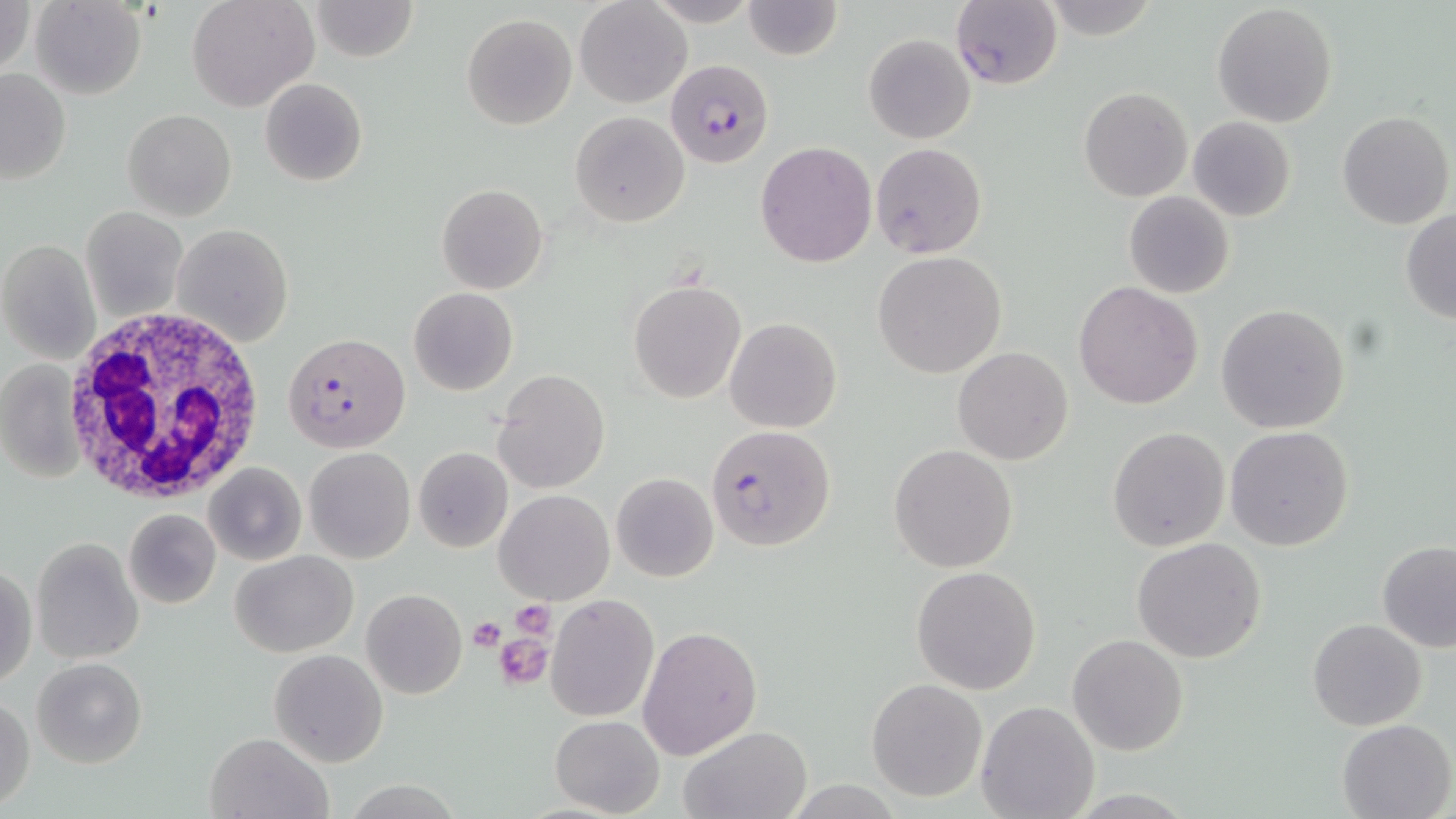

Approximate bounding boxes as (x1, y1, x2, y2) in pixels. Uninfected red blood cell locations: (1, 0, 34, 79), (31, 0, 147, 99), (187, 0, 319, 113), (311, 0, 418, 61), (574, 0, 691, 108), (648, 0, 761, 28), (741, 1, 844, 60), (1211, 3, 1339, 127), (462, 12, 578, 130), (864, 35, 974, 145), (0, 67, 71, 185), (260, 77, 368, 187), (1079, 87, 1192, 201), (122, 109, 236, 222), (1336, 110, 1453, 229), (570, 111, 689, 226), (1188, 116, 1296, 222), (755, 140, 876, 267), (869, 141, 989, 260), (436, 183, 549, 295), (1123, 191, 1235, 299), (81, 207, 188, 322), (1401, 211, 1456, 323), (172, 223, 294, 349), (0, 238, 100, 364), (873, 252, 1006, 377), (628, 279, 746, 403), (1073, 280, 1203, 409), (408, 287, 518, 395), (1214, 303, 1352, 434), (725, 317, 841, 432), (953, 347, 1073, 465), (2, 360, 85, 484), (494, 368, 609, 494), (1225, 425, 1353, 551), (1108, 426, 1230, 552), (889, 445, 1017, 572), (305, 447, 415, 563), (413, 447, 513, 552), (202, 461, 307, 566), (610, 472, 718, 581), (495, 489, 614, 604), (124, 509, 220, 608), (31, 537, 143, 665), (1132, 537, 1267, 664), (1375, 539, 1456, 653), (231, 549, 358, 658), (1, 562, 36, 690), (911, 565, 1042, 694), (361, 589, 468, 699), (546, 594, 660, 723), (1307, 619, 1428, 731), (638, 625, 762, 759), (1067, 634, 1188, 756), (269, 649, 389, 767), (31, 656, 148, 769), (867, 678, 987, 802), (1, 695, 35, 809), (975, 700, 1099, 819), (549, 714, 663, 817), (1336, 718, 1456, 818), (679, 726, 812, 819), (205, 731, 330, 818). Plasmodium falciparum-infected red blood cell locations: (951, 2, 1062, 88), (665, 58, 775, 168), (283, 335, 411, 453), (706, 424, 837, 551). White blood cell locations: (65, 308, 267, 506), (1, 364, 90, 489). Platelet locations: (512, 600, 553, 637), (467, 616, 507, 653), (494, 632, 550, 689). Slide-level diagnosis: Plasmodium falciparum. 1000x magnification. Thin blood smear. Image is 1456×819 pixels. One field of a larger specimen. May-Grünwald-Giemsa-stained preparation. Light microscopy.